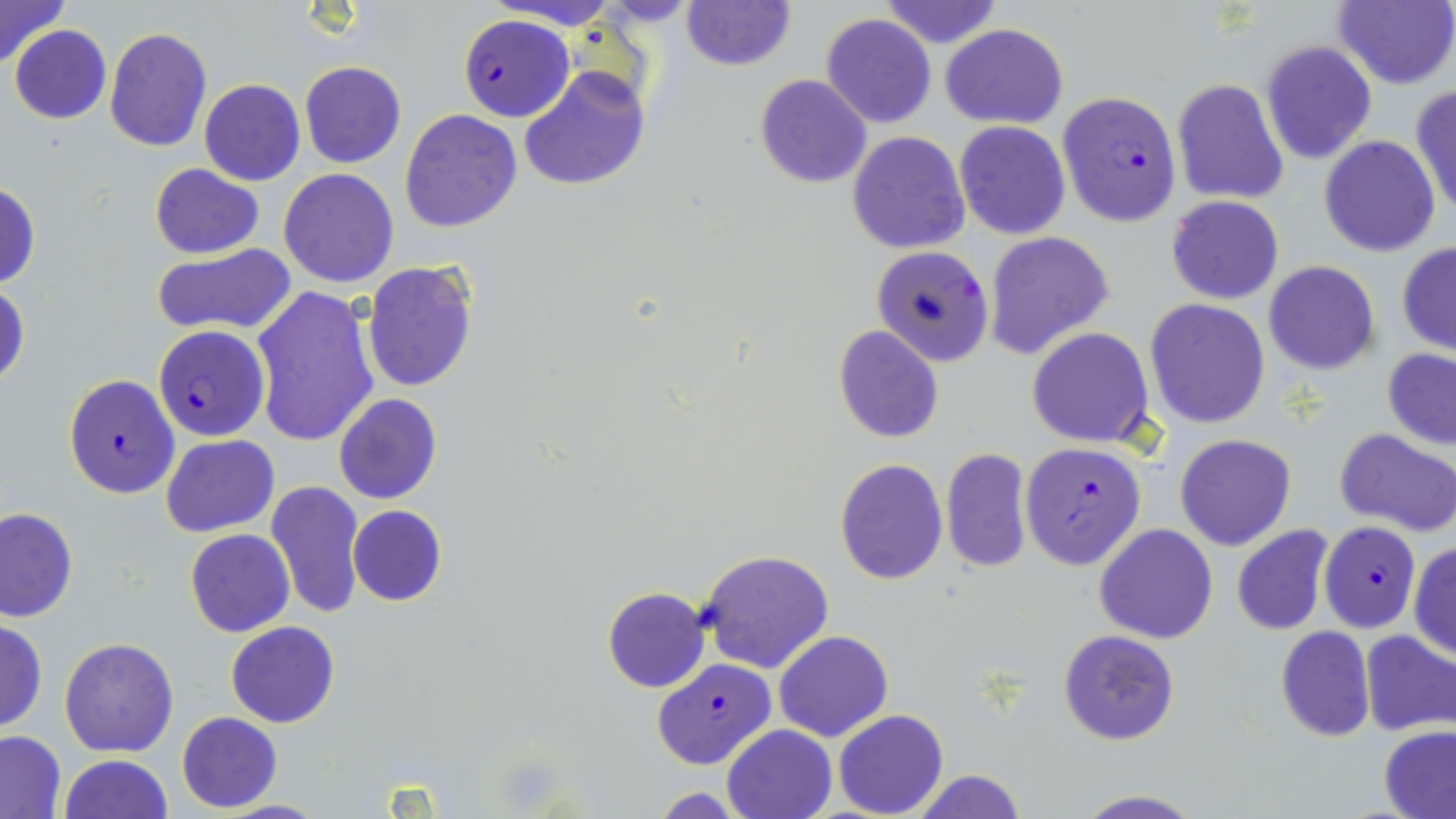
Summary:
  - Coordinate format: approximate bounding boxes as (x1,y1)-(x2,y2) corner pairs in pixels
  - Uninfected red blood cell locations: (2,0)-(68,67), (487,0)-(623,30), (876,0)-(1004,49), (1332,0)-(1456,90), (681,1)-(795,71), (820,13)-(937,128), (940,23)-(1068,129), (9,24)-(111,124), (104,27)-(213,152), (1259,40)-(1377,165), (299,62)-(405,168), (519,66)-(651,191), (754,75)-(872,188), (1171,78)-(1289,204), (200,79)-(305,185), (1409,84)-(1456,217), (399,109)-(523,232), (954,120)-(1070,239), (846,130)-(970,255), (1319,135)-(1441,257), (149,164)-(263,258), (278,167)-(399,288), (0,184)-(41,289), (1166,195)-(1284,305), (984,231)-(1115,359), (1396,242)-(1456,356), (151,243)-(297,337), (363,261)-(480,393), (1263,261)-(1380,375), (0,281)-(29,391), (251,284)-(379,449), (1145,298)-(1271,429), (832,325)-(944,444), (1027,327)-(1154,448), (1382,347)-(1455,450), (334,393)-(442,506), (1334,428)-(1456,536), (161,434)-(278,536), (1174,434)-(1296,551), (940,447)-(1035,576), (835,457)-(948,585), (266,480)-(364,619), (348,505)-(447,607), (1,507)-(77,622), (1094,523)-(1219,644), (1230,525)-(1336,636), (185,529)-(295,638), (1409,543)-(1456,659), (698,549)-(835,674), (602,588)-(709,693), (0,618)-(47,733), (227,621)-(340,727), (1275,625)-(1376,742), (1059,629)-(1180,745), (1359,629)-(1455,735), (773,631)-(894,742), (59,637)-(179,756), (833,710)-(949,819), (176,711)-(283,812), (722,725)-(836,818), (1378,725)-(1456,819), (0,731)-(64,818), (59,754)-(174,819), (910,770)-(1027,818), (651,789)-(748,819), (1069,790)-(1207,819)
  - Plasmodium falciparum-infected red blood cell locations: (456,17)-(576,122), (1057,92)-(1181,226), (872,246)-(994,366), (153,325)-(271,442), (63,373)-(179,498), (1019,442)-(1147,570), (1314,521)-(1422,632), (652,658)-(776,768)
  - Slide-level diagnosis: Plasmodium falciparum
  - Preparation: thin blood smear
  - Stain: May-Grünwald-Giemsa
  - Field of view: single
  - Modality: light microscopy
  - Magnification: 1000x
  - Image size: 1456×819 pixels